Classify this cell by malaria status.
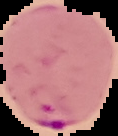

It is parasitized.

Summary:
  - Image type: segmented cell region with the area outside set to black
  - Image size: 118×136 pixels
  - Preparation: thin blood film